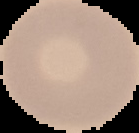

The area outside the segmented cell region is set to black. Malaria status: uninfected. Image is 139×133 pixels. From a thin blood film.